State which parasite is depicted.
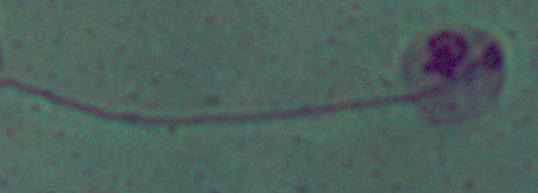
Leishmania.

Photomicrograph. 1000x magnification.